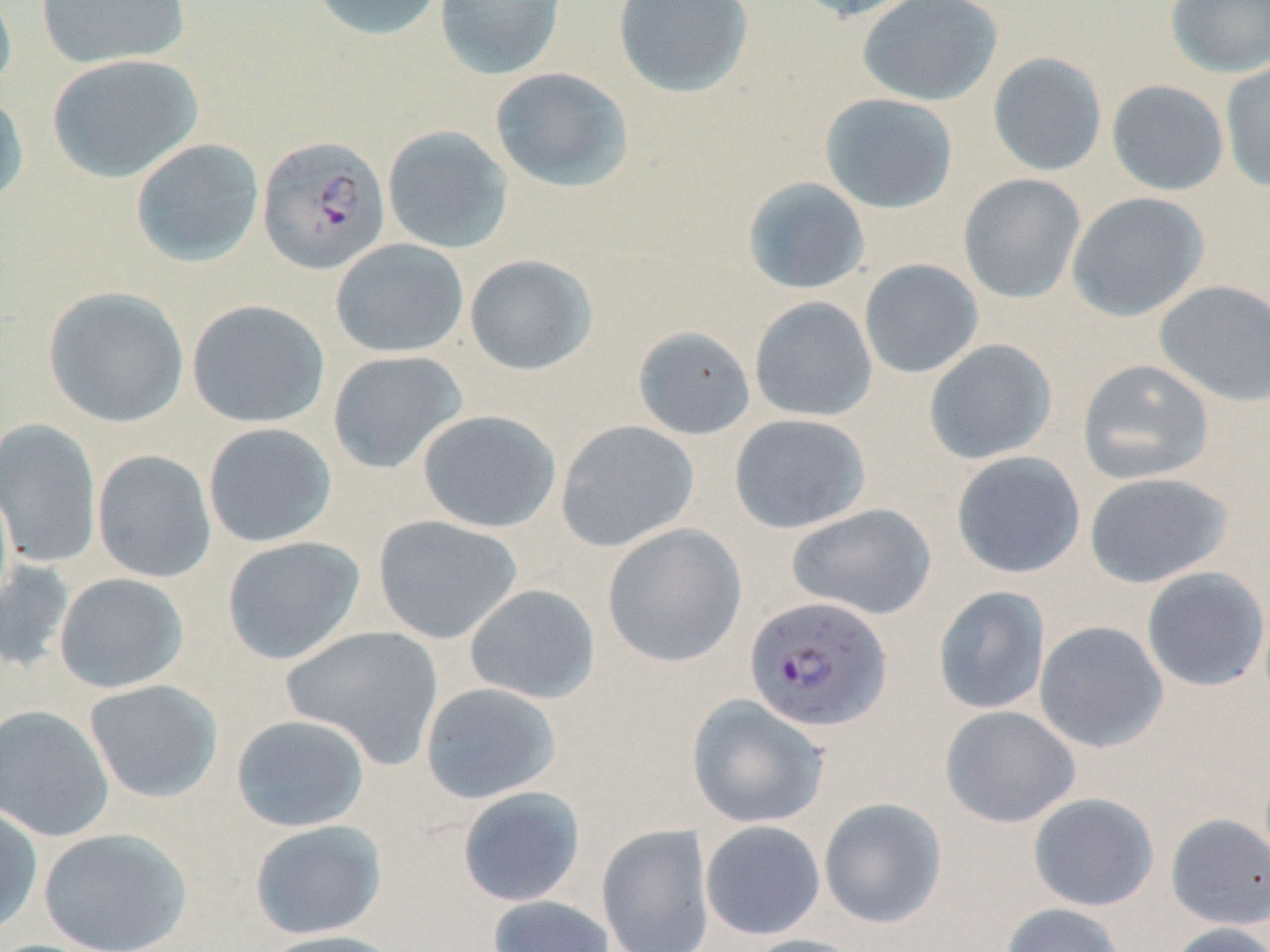

Approximate bounding boxes as (x1, y1, x2, y2) in pixels. Uninfected red blood cell locations: (35, 0, 191, 71), (311, 0, 446, 42), (434, 0, 567, 81), (613, 0, 753, 98), (788, 0, 923, 21), (857, 0, 1002, 107), (1166, 0, 1270, 78), (0, 2, 17, 98), (987, 52, 1107, 177), (46, 53, 203, 183), (1219, 60, 1270, 192), (490, 66, 635, 193), (1106, 80, 1229, 196), (0, 90, 30, 211), (820, 93, 958, 214), (382, 125, 514, 254), (130, 138, 265, 268), (958, 173, 1086, 303), (741, 177, 871, 295), (1066, 192, 1210, 322), (331, 239, 469, 359), (464, 254, 598, 376), (859, 258, 984, 379), (1154, 280, 1270, 407), (43, 286, 189, 428), (749, 296, 878, 423), (186, 299, 330, 429), (632, 325, 756, 440), (923, 338, 1057, 464), (327, 351, 468, 475), (1077, 359, 1214, 485), (417, 409, 562, 533), (728, 413, 871, 534), (0, 418, 102, 569), (555, 420, 699, 552), (203, 422, 338, 548), (92, 450, 217, 583), (951, 451, 1086, 579), (1083, 471, 1233, 588), (0, 481, 14, 611), (786, 504, 937, 620), (373, 515, 523, 645), (602, 523, 747, 668), (221, 535, 366, 665), (0, 558, 76, 676), (1141, 567, 1269, 692), (53, 573, 190, 693), (464, 584, 601, 704), (933, 586, 1051, 715), (1034, 620, 1169, 753), (281, 626, 445, 769), (84, 679, 224, 803), (419, 682, 562, 804), (686, 694, 830, 829), (0, 704, 115, 842), (939, 705, 1081, 828), (231, 714, 370, 833), (457, 786, 586, 908), (1028, 792, 1159, 911), (819, 797, 948, 928), (0, 804, 44, 936), (1165, 813, 1270, 929), (249, 819, 387, 940), (700, 820, 826, 940), (595, 823, 716, 952), (38, 827, 192, 952), (487, 895, 615, 952), (1000, 902, 1127, 952), (1164, 922, 1270, 952), (254, 929, 404, 952), (741, 934, 868, 952). Plasmodium falciparum-infected red blood cell locations: (256, 135, 391, 275), (744, 596, 892, 732). Slide-level diagnosis: Plasmodium falciparum. One field of a larger specimen. Thin blood film. May-Grünwald-Giemsa stain. Captured at 1000x magnification. Image is 1270×952 pixels. Light microscopy.